Identify the parasite.
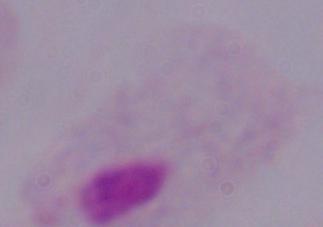

A trichomonad.

Summary:
  - Magnification: 1000x
  - Modality: photomicrograph